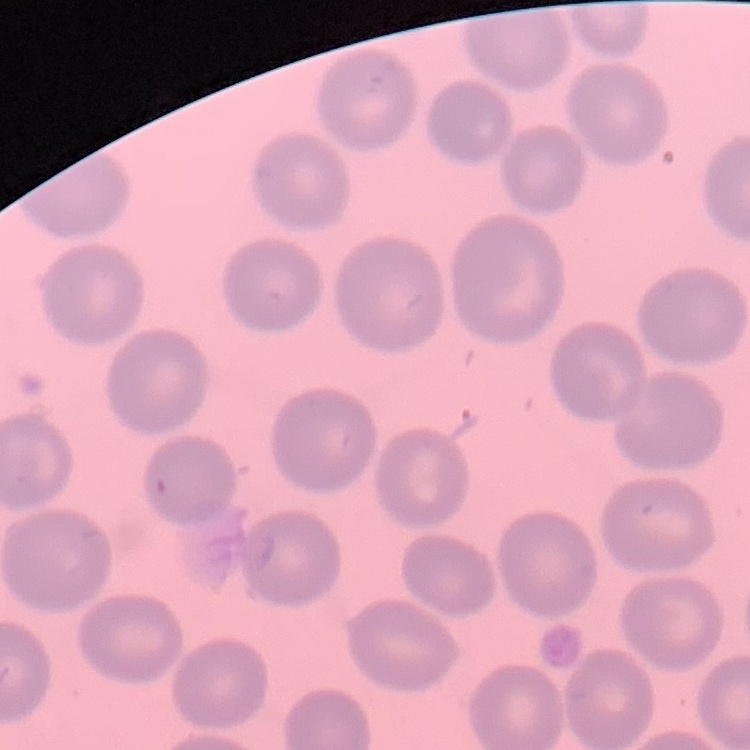
erythrocyte morphology = no rouleaux formation
stain = Field's or Giemsa
image type = square crop of a larger photomicrograph
preparation = thin blood film